Comment on the morphology of the red blood cells.
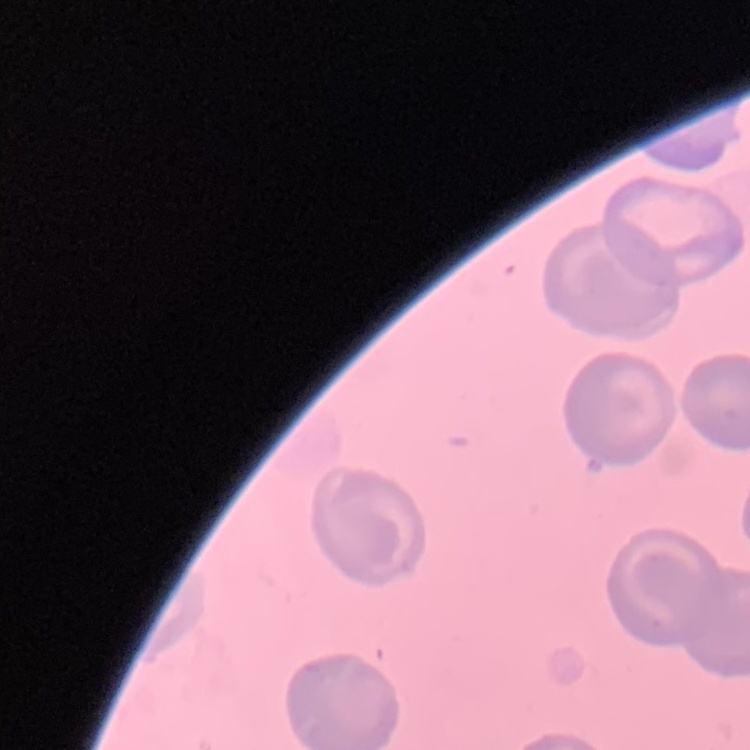

They show no rouleaux formation.

One tile cut from a larger photomicrograph. Stained with either Field's or Giemsa. Thin blood film.